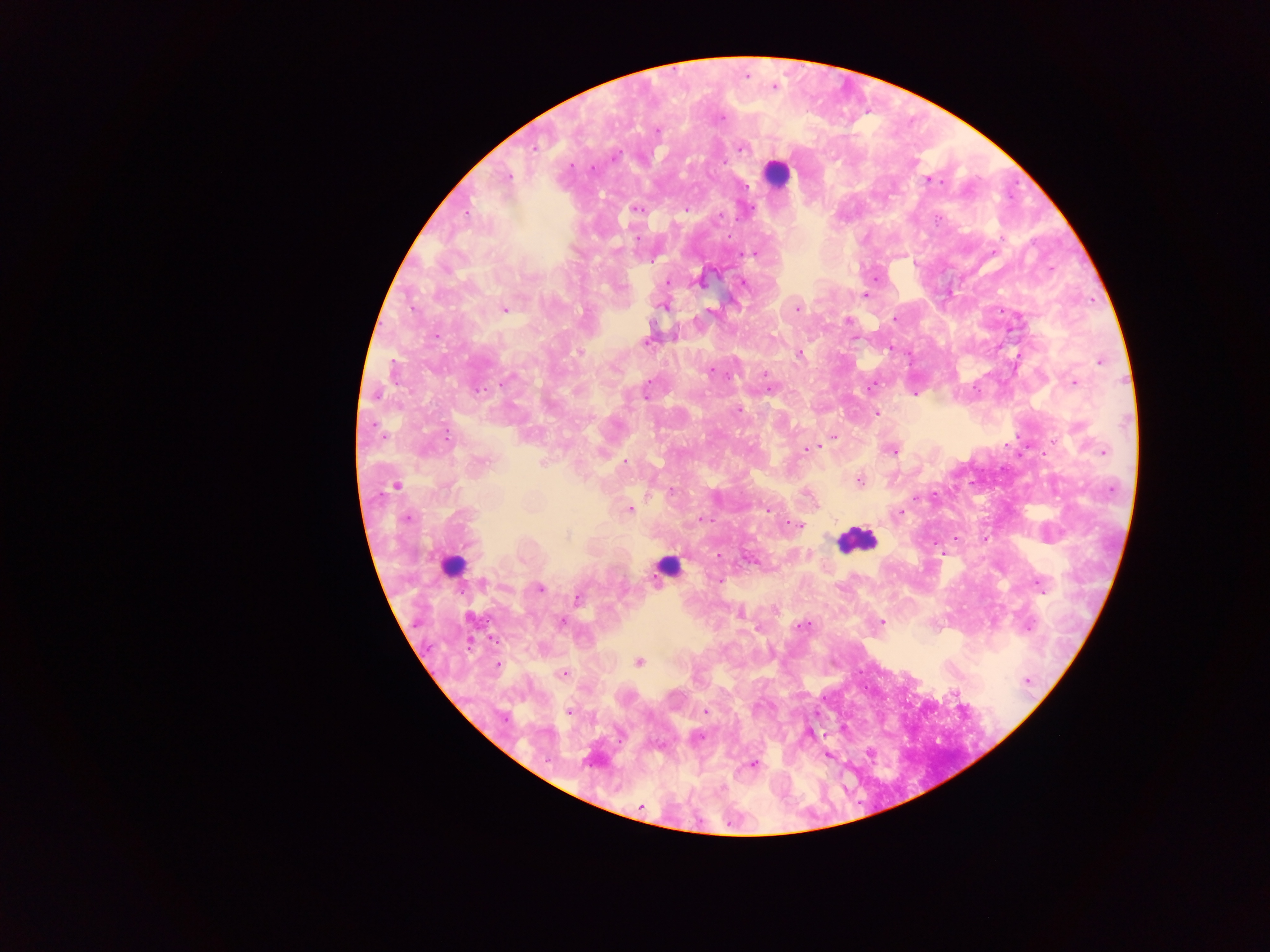

Approximate centers as (x, y) in pixels.
Summary:
  - Leukocyte locations: (776, 172), (856, 540), (452, 547), (667, 567)
  - Malaria parasite locations: (745, 74), (774, 86), (657, 130), (533, 147), (741, 147), (614, 157), (592, 169), (508, 177), (929, 180), (636, 208), (686, 209), (719, 217), (756, 253), (876, 278), (743, 282), (667, 283), (865, 295), (664, 305), (797, 308), (503, 309), (895, 319), (847, 320), (647, 341), (580, 351), (798, 354), (1099, 360), (710, 371), (764, 375), (1074, 383), (873, 385), (915, 393), (738, 408), (876, 412), (446, 434), (833, 438), (823, 444), (807, 448), (891, 449), (1103, 452), (544, 462), (480, 463), (624, 464), (859, 479), (396, 485), (932, 495), (629, 509), (766, 509), (898, 512), (406, 518), (701, 518), (798, 526), (984, 539), (941, 551), (718, 554), (719, 581), (1039, 585), (540, 588), (577, 598), (739, 612), (561, 622), (881, 622), (802, 626), (757, 629), (638, 662), (497, 663), (563, 674), (1026, 680), (953, 692), (705, 711), (569, 712), (809, 733), (697, 736), (869, 752), (827, 754), (752, 764)
  - Image size: 1270×952 pixels
  - Capture: mobile-phone photograph through a microscope
  - Preparation: thick blood film
  - Country: Ghana
  - Field of view: single